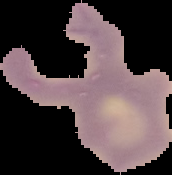

Summary:
  - Image size: 172×175 pixels
  - Preparation: thin blood film
  - Image type: cell region segmented out of the field of view; surrounding area masked to black
  - Result: Plasmodium parasites detected